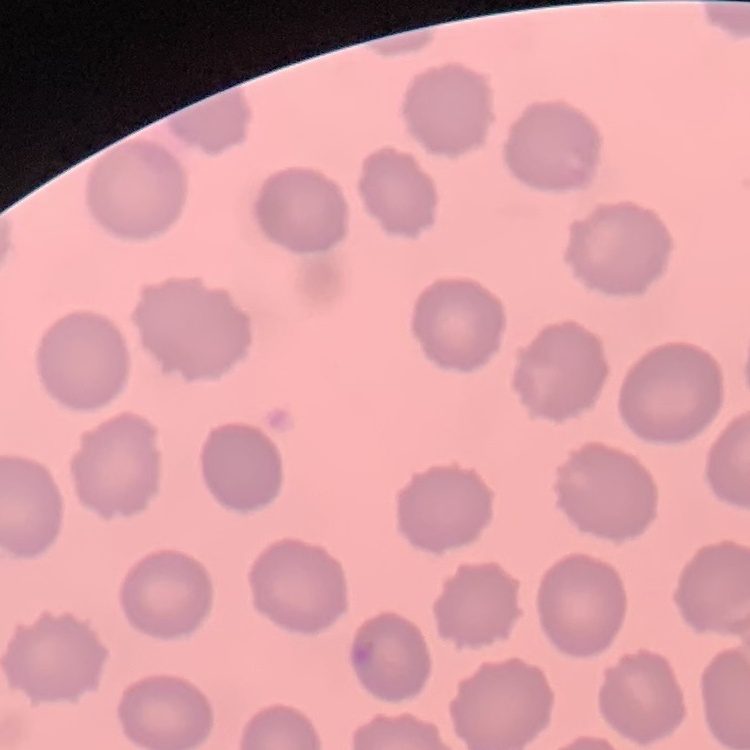

Summary:
  - Erythrocyte morphology: no rouleaux formation
  - Image type: one tile cut from a larger photomicrograph
  - Preparation: thin blood smear
  - Stain: Field's or Giemsa